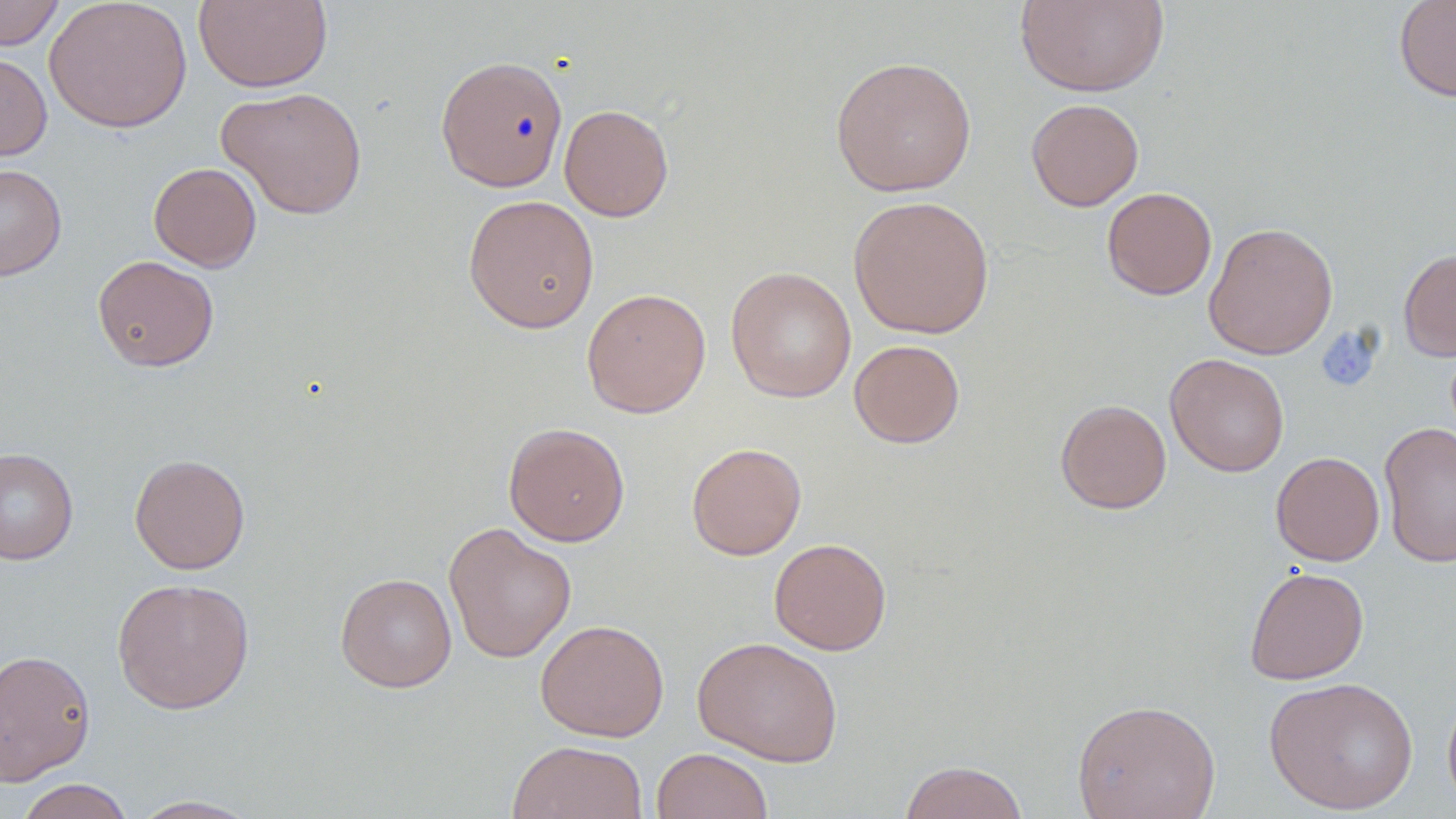

Summary:
  - Coordinate format: approximate bounding boxes as [x1, y1, x2, y2] in pixels
  - Uninfected red blood cell locations: [0, 0, 65, 51], [44, 0, 193, 133], [1014, 0, 1170, 98], [1394, 0, 1456, 103], [194, 1, 332, 92], [0, 51, 52, 161], [435, 55, 569, 192], [830, 56, 976, 197], [217, 86, 368, 219], [1026, 98, 1144, 211], [559, 104, 674, 222], [148, 162, 262, 272], [0, 163, 67, 281], [1102, 187, 1217, 300], [462, 194, 600, 333], [848, 195, 994, 339], [1203, 222, 1339, 360], [1398, 247, 1456, 362], [92, 255, 219, 372], [725, 265, 856, 403], [581, 287, 711, 418], [849, 340, 965, 448], [1164, 353, 1290, 477], [1055, 399, 1172, 514], [1379, 421, 1456, 568], [504, 422, 630, 546], [686, 442, 807, 559], [0, 447, 79, 565], [1270, 451, 1385, 566], [129, 453, 250, 575], [444, 521, 576, 663], [769, 538, 892, 655], [1244, 566, 1369, 685], [335, 573, 457, 692], [111, 577, 255, 714], [535, 619, 670, 741], [692, 635, 843, 767], [0, 648, 96, 785], [1264, 675, 1419, 814], [1442, 684, 1456, 815], [1072, 698, 1221, 819], [507, 740, 647, 819], [651, 747, 774, 819], [899, 760, 1030, 819], [15, 779, 135, 819], [127, 795, 265, 818]
  - Platelet locations: [1328, 330, 1380, 386]
  - Slide-level diagnosis: no evidence of blood parasites
  - Preparation: thin blood film
  - Image size: 1456×819 pixels
  - Modality: light microscopy
  - Field of view: one of a larger specimen
  - Stain: May-Grünwald-Giemsa
  - Magnification: 1000x